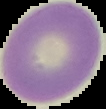

preparation = thin blood smear
image type = cell region segmented out of the field of view; surrounding area masked to black
image size = 106×109 pixels
malaria status = uninfected